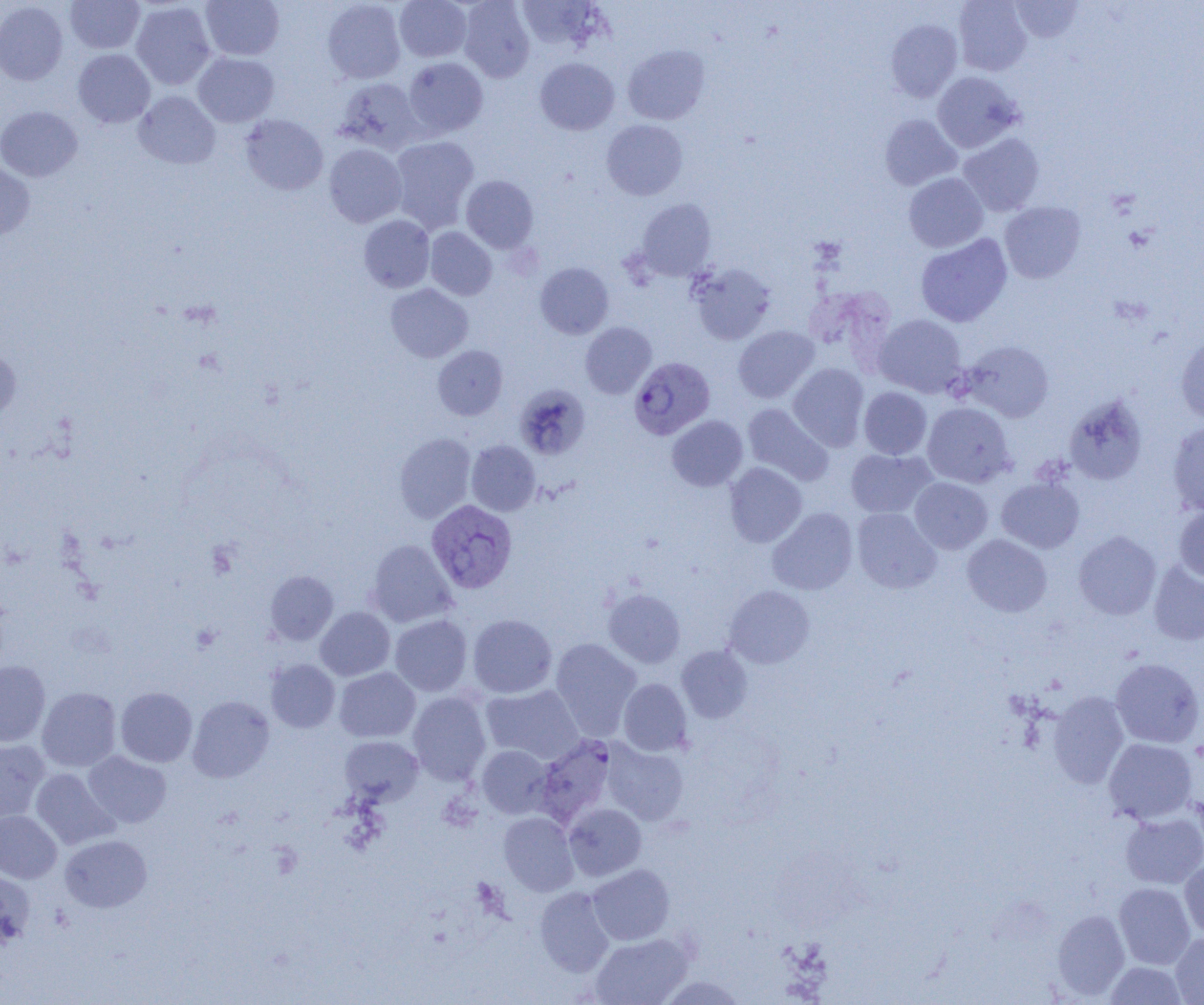

{
  "slide_level_diagnosis": "Plasmodium vivax",
  "preparation": "thin blood smear",
  "modality": "optical microscopy",
  "image_size": "1204×1005 pixels",
  "plasmodium_vivax_infected_red_blood_cell_locations": "approximate bounding boxes as (x1,y1)-(x2,y2) corner pairs in pixels: (629,356)-(715,439), (426,500)-(517,594)",
  "magnification": "1000x",
  "field_of_view": "single",
  "uninfected_red_blood_cell_locations": "approximate bounding boxes as (x1,y1)-(x2,y2) corner pairs in pixels: (65,0)-(145,54), (201,0)-(285,61), (322,0)-(406,84), (394,0)-(471,62), (458,0)-(535,82), (516,0)-(605,53), (1009,0)-(1084,43), (0,1)-(68,85), (131,1)-(216,90), (953,1)-(1032,76), (886,19)-(962,101), (622,45)-(710,125), (72,49)-(155,128), (193,52)-(279,127), (403,57)-(488,137), (535,58)-(619,135), (932,72)-(1022,153), (333,78)-(425,154), (134,91)-(220,169), (0,105)-(82,182), (240,114)-(328,195), (880,114)-(962,189), (601,119)-(688,200), (957,133)-(1044,216), (389,136)-(479,232), (324,144)-(407,227), (0,161)-(35,243), (903,172)-(988,252), (461,175)-(538,252), (636,199)-(717,281), (999,201)-(1086,283), (359,215)-(435,293), (425,227)-(497,300), (915,234)-(1012,327), (535,262)-(614,339), (688,262)-(776,345), (386,283)-(473,362), (874,314)-(968,398), (580,322)-(656,398), (733,325)-(819,402), (1175,333)-(1204,425), (962,340)-(1054,422), (433,345)-(508,420), (0,348)-(21,422), (788,363)-(869,451), (515,384)-(590,459), (859,386)-(932,459), (1063,395)-(1149,485), (922,402)-(1015,487), (742,403)-(833,486), (667,415)-(748,491), (1167,421)-(1204,515), (394,433)-(476,523), (467,440)-(540,515), (845,448)-(936,518), (725,462)-(807,548), (996,476)-(1084,553), (909,477)-(993,553), (1174,505)-(1204,583), (768,508)-(858,595), (852,508)-(941,593), (1073,530)-(1161,620), (962,534)-(1052,617), (366,539)-(457,627), (1147,560)-(1204,646), (265,570)-(338,644), (724,585)-(815,668), (603,588)-(685,668), (315,607)-(395,681), (390,614)-(472,696), (468,614)-(557,698), (550,638)-(641,739), (677,645)-(752,723), (1110,658)-(1204,748), (266,659)-(340,732), (0,661)-(50,746), (334,667)-(420,742), (618,678)-(692,756), (481,684)-(583,763), (37,687)-(121,772), (115,687)-(197,767), (408,691)-(491,785), (1048,691)-(1130,788), (188,696)-(274,782), (340,736)-(423,805), (534,736)-(616,826), (1103,738)-(1197,824), (0,739)-(50,824), (603,740)-(689,825), (477,745)-(553,818), (83,751)-(171,828), (31,768)-(119,849), (563,803)-(646,881), (0,810)-(62,883), (1120,811)-(1204,888), (499,812)-(579,896), (60,835)-(152,912), (1180,859)-(1204,939), (588,864)-(675,945), (0,871)-(36,950), (1114,882)-(1195,969), (534,887)-(614,976), (1052,909)-(1130,999), (589,933)-(692,1005), (1170,933)-(1204,1004), (1105,961)-(1188,1005), (658,974)-(748,1005)"
}